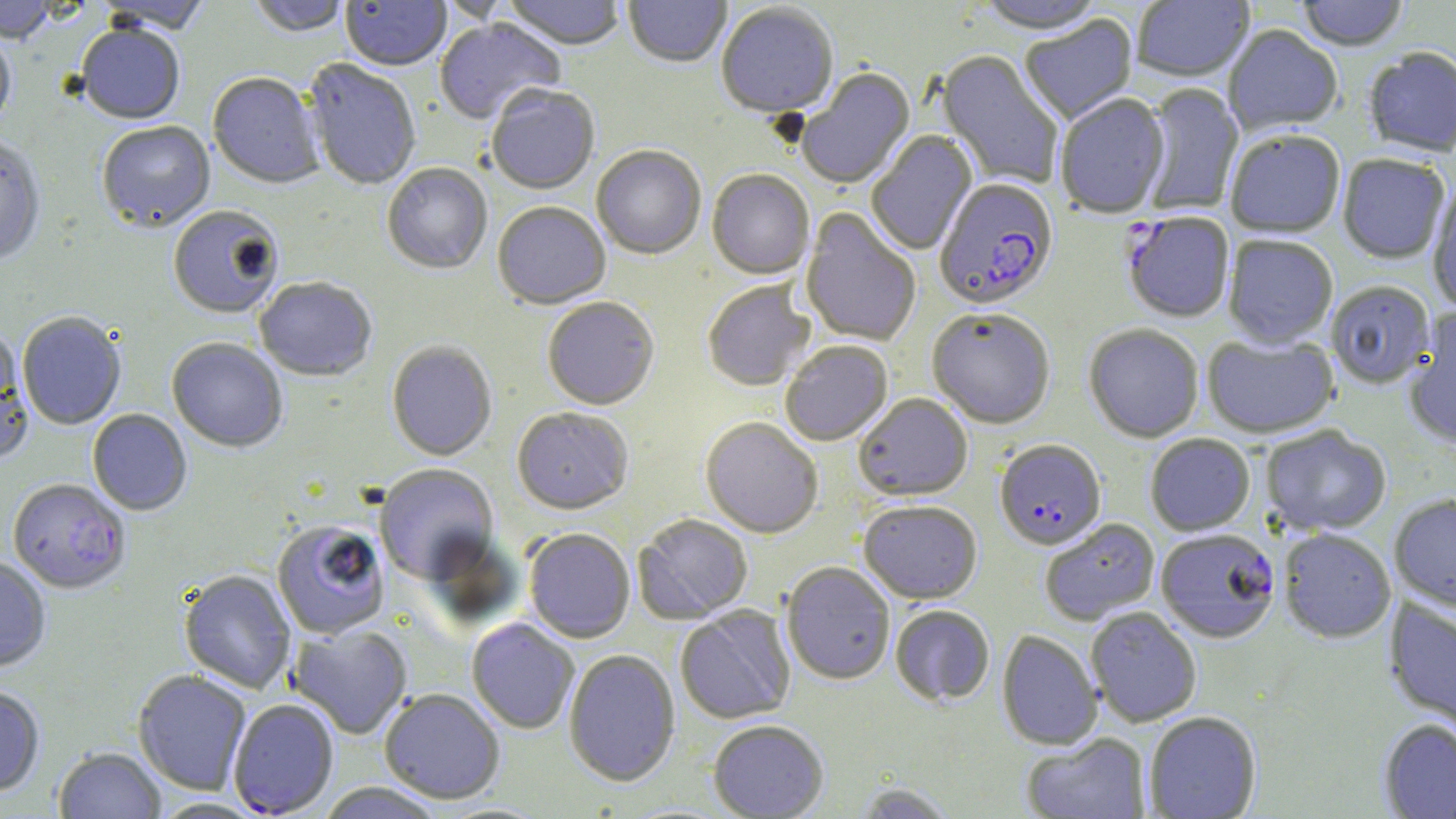

slide-level diagnosis = Plasmodium falciparum
image size = 1456×819 pixels
modality = optical microscopy
Plasmodium falciparum-infected red blood cell locations = approximate bounding boxes as named x1/y1/x2/y2 corners in pixels: (x1=934, y1=180, x2=1059, y2=314), (x1=1122, y1=213, x2=1235, y2=325), (x1=995, y1=441, x2=1106, y2=552), (x1=7, y1=480, x2=131, y2=596), (x1=1156, y1=530, x2=1280, y2=644)
field of view = single
stain = May-Grünwald-Giemsa
uninfected red blood cell locations = approximate bounding boxes as named x1/y1/x2/y2 corners in pixels: (x1=248, y1=0, x2=352, y2=39), (x1=502, y1=0, x2=626, y2=53), (x1=623, y1=0, x2=731, y2=69), (x1=973, y1=0, x2=1109, y2=37), (x1=1131, y1=0, x2=1254, y2=84), (x1=1296, y1=0, x2=1410, y2=53), (x1=0, y1=1, x2=58, y2=45), (x1=94, y1=1, x2=213, y2=37), (x1=340, y1=1, x2=451, y2=73), (x1=716, y1=4, x2=839, y2=120), (x1=1020, y1=16, x2=1139, y2=126), (x1=434, y1=18, x2=566, y2=127), (x1=1223, y1=25, x2=1342, y2=138), (x1=76, y1=26, x2=185, y2=126), (x1=0, y1=30, x2=16, y2=137), (x1=1363, y1=49, x2=1456, y2=158), (x1=936, y1=51, x2=1063, y2=190), (x1=303, y1=60, x2=421, y2=191), (x1=797, y1=69, x2=916, y2=191), (x1=207, y1=74, x2=324, y2=191), (x1=1140, y1=84, x2=1243, y2=216), (x1=486, y1=87, x2=600, y2=197), (x1=1056, y1=94, x2=1171, y2=221), (x1=97, y1=123, x2=216, y2=235), (x1=866, y1=131, x2=978, y2=256), (x1=1225, y1=132, x2=1345, y2=239), (x1=0, y1=138, x2=46, y2=267), (x1=592, y1=147, x2=706, y2=262), (x1=1337, y1=155, x2=1451, y2=265), (x1=382, y1=164, x2=492, y2=276), (x1=707, y1=171, x2=815, y2=282), (x1=1427, y1=185, x2=1456, y2=313), (x1=493, y1=204, x2=611, y2=311), (x1=167, y1=207, x2=284, y2=321), (x1=800, y1=208, x2=921, y2=347), (x1=1223, y1=236, x2=1338, y2=350), (x1=254, y1=279, x2=377, y2=383), (x1=702, y1=282, x2=815, y2=392), (x1=1327, y1=282, x2=1436, y2=390), (x1=542, y1=299, x2=659, y2=412), (x1=927, y1=310, x2=1055, y2=431), (x1=1403, y1=310, x2=1456, y2=450), (x1=18, y1=313, x2=127, y2=431), (x1=1084, y1=325, x2=1204, y2=443), (x1=0, y1=329, x2=34, y2=468), (x1=1202, y1=334, x2=1340, y2=439), (x1=167, y1=339, x2=288, y2=453), (x1=781, y1=342, x2=893, y2=447), (x1=387, y1=343, x2=497, y2=462), (x1=854, y1=394, x2=973, y2=502), (x1=87, y1=409, x2=192, y2=516), (x1=512, y1=409, x2=633, y2=517), (x1=700, y1=418, x2=823, y2=540), (x1=1261, y1=426, x2=1391, y2=537), (x1=1145, y1=435, x2=1255, y2=537), (x1=375, y1=465, x2=498, y2=585), (x1=1389, y1=495, x2=1456, y2=615), (x1=859, y1=502, x2=982, y2=605), (x1=633, y1=515, x2=753, y2=625), (x1=1041, y1=519, x2=1160, y2=626), (x1=271, y1=522, x2=390, y2=640), (x1=1279, y1=529, x2=1396, y2=644), (x1=524, y1=530, x2=635, y2=644), (x1=0, y1=557, x2=51, y2=672), (x1=781, y1=563, x2=895, y2=686), (x1=179, y1=570, x2=296, y2=694), (x1=1384, y1=598, x2=1456, y2=735), (x1=676, y1=605, x2=796, y2=725), (x1=890, y1=606, x2=995, y2=707), (x1=1085, y1=608, x2=1201, y2=727), (x1=466, y1=618, x2=579, y2=735), (x1=288, y1=626, x2=413, y2=740), (x1=997, y1=630, x2=1103, y2=751), (x1=564, y1=650, x2=680, y2=788), (x1=133, y1=671, x2=251, y2=796), (x1=0, y1=686, x2=45, y2=798), (x1=379, y1=690, x2=505, y2=805), (x1=228, y1=700, x2=339, y2=817), (x1=1144, y1=712, x2=1262, y2=818), (x1=1378, y1=719, x2=1456, y2=818), (x1=708, y1=721, x2=829, y2=818), (x1=1021, y1=733, x2=1151, y2=818), (x1=53, y1=748, x2=167, y2=819), (x1=851, y1=782, x2=959, y2=818), (x1=314, y1=783, x2=447, y2=819), (x1=150, y1=798, x2=268, y2=818)
magnification = 1000x
preparation = thin blood smear